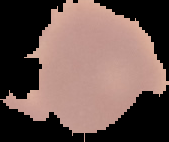

preparation = thin blood film
result = negative for malaria parasites
image type = segmented cell region on a black background
image size = 169×142 pixels